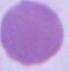

Captured at 1000x magnification. Micrograph. An erythrocyte is seen.